Classify this cell by malaria status.
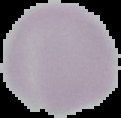

Uninfected.

image_size: 121×118 pixels
preparation: thin blood film
image_type: segmented cell region with the area outside set to black